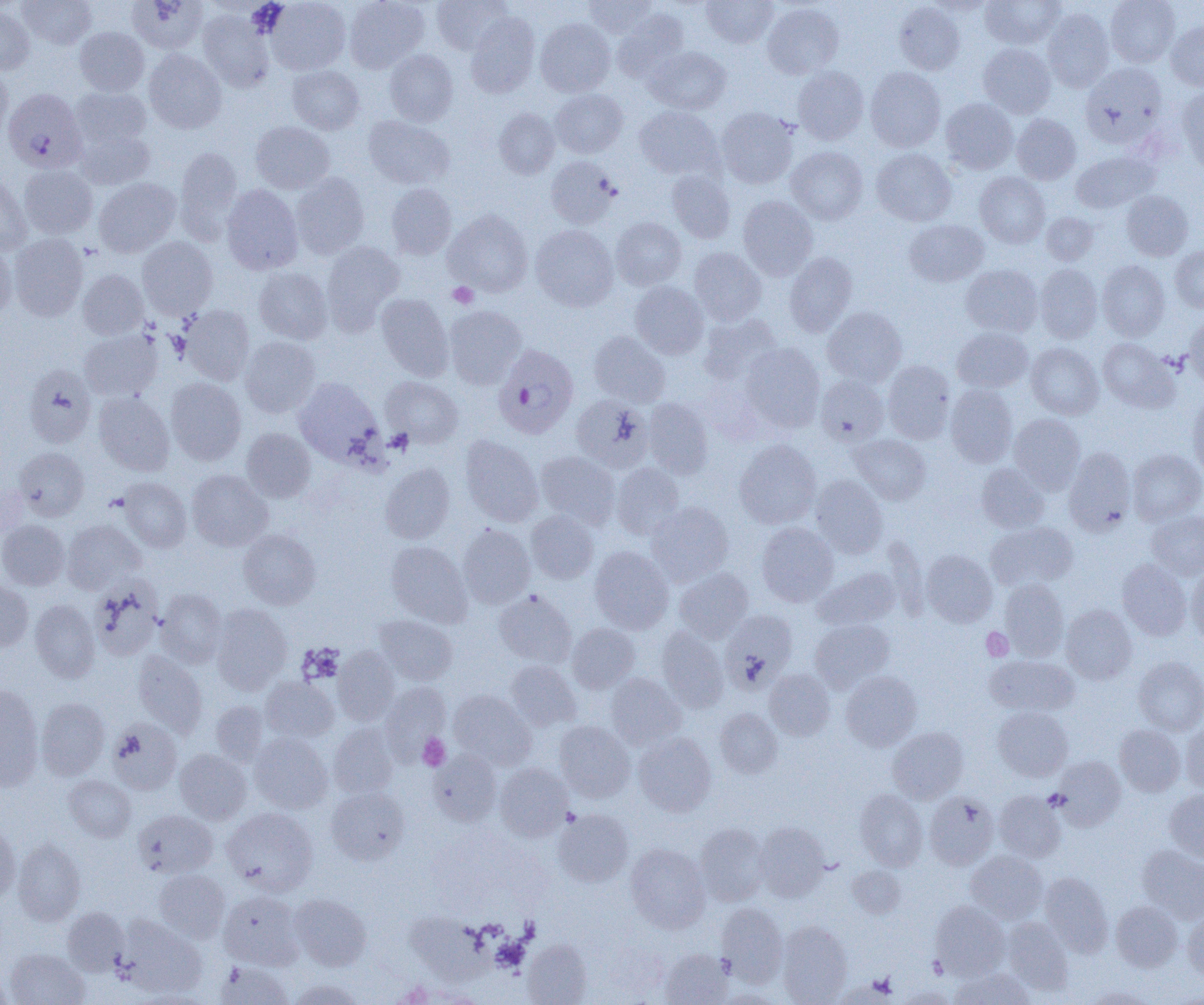
Summary:
  - Coordinate format: approximate bounding boxes as [x1, y1, x2, y2] in pixels
  - Platelet locations: [447, 282, 478, 309], [981, 627, 1013, 661], [417, 734, 450, 770], [1044, 789, 1068, 811], [859, 973, 899, 999]
  - Plasmodium falciparum-infected red blood cell locations: [3, 88, 87, 173], [493, 345, 579, 440]
  - Uninfected red blood cell locations: [17, 0, 96, 49], [127, 0, 208, 54], [265, 0, 350, 75], [345, 0, 429, 73], [432, 0, 511, 54], [582, 0, 659, 37], [700, 0, 778, 47], [927, 0, 994, 17], [980, 0, 1064, 49], [1105, 0, 1180, 67], [762, 2, 844, 79], [894, 2, 965, 74], [0, 5, 35, 74], [1042, 7, 1114, 92], [613, 8, 691, 83], [198, 10, 275, 92], [466, 13, 540, 97], [535, 18, 615, 96], [1166, 21, 1204, 91], [75, 27, 149, 95], [978, 43, 1056, 118], [646, 46, 731, 114], [144, 49, 226, 133], [385, 50, 458, 126], [1081, 63, 1167, 148], [0, 65, 13, 139], [287, 65, 364, 134], [792, 66, 869, 144], [865, 67, 946, 152], [70, 87, 152, 151], [550, 88, 627, 158], [1177, 88, 1204, 176], [941, 97, 1018, 174], [634, 106, 722, 179], [493, 107, 560, 179], [716, 107, 799, 188], [1012, 114, 1081, 184], [363, 116, 454, 189], [250, 121, 335, 194], [74, 127, 155, 189], [175, 146, 243, 238], [786, 146, 868, 224], [871, 148, 956, 226], [1071, 150, 1158, 213], [546, 156, 620, 228], [18, 164, 98, 239], [666, 170, 735, 243], [0, 172, 33, 255], [975, 172, 1050, 248], [291, 173, 369, 259], [94, 178, 181, 257], [386, 183, 457, 259], [221, 184, 303, 274], [1121, 190, 1193, 260], [738, 196, 818, 279], [443, 210, 533, 296], [1041, 212, 1099, 265], [610, 217, 686, 290], [904, 219, 988, 287], [530, 224, 618, 311], [9, 233, 88, 321], [137, 236, 218, 319], [0, 239, 17, 322], [321, 241, 405, 332], [1171, 246, 1204, 312], [689, 247, 766, 326], [784, 252, 857, 336], [1097, 260, 1170, 341], [961, 264, 1042, 336], [1035, 264, 1102, 343], [254, 267, 333, 344], [78, 270, 149, 340], [630, 281, 709, 358], [376, 293, 454, 381], [179, 305, 255, 385], [444, 305, 526, 389], [823, 307, 906, 387], [699, 313, 782, 385], [1184, 313, 1204, 388], [952, 327, 1033, 392], [79, 329, 162, 401], [589, 332, 670, 407], [240, 336, 320, 417], [1098, 338, 1177, 413], [741, 343, 825, 433], [1026, 343, 1103, 419], [882, 361, 954, 443], [23, 364, 97, 447], [815, 375, 888, 445], [381, 376, 464, 448], [294, 377, 382, 464], [166, 378, 246, 465], [945, 384, 1017, 467], [94, 391, 175, 475], [1187, 393, 1204, 480], [572, 395, 653, 472], [643, 398, 714, 478], [1009, 413, 1084, 494], [242, 428, 316, 502], [849, 434, 930, 505], [460, 435, 543, 526], [734, 439, 821, 529], [14, 447, 89, 520], [1064, 447, 1135, 535], [1128, 449, 1204, 525], [536, 451, 620, 528], [380, 463, 455, 543], [611, 463, 684, 539], [976, 463, 1050, 533], [186, 470, 273, 551], [810, 475, 888, 558], [119, 478, 192, 552], [646, 502, 733, 585], [526, 510, 599, 584], [1146, 510, 1204, 579], [61, 519, 146, 594], [0, 520, 69, 590], [986, 521, 1077, 591], [756, 522, 839, 607], [457, 524, 535, 608], [238, 529, 320, 609], [385, 541, 472, 627], [589, 546, 674, 634], [921, 549, 997, 627], [1117, 559, 1191, 640], [1186, 565, 1204, 646], [674, 567, 753, 641], [813, 567, 900, 631], [90, 575, 163, 660], [999, 579, 1069, 660], [0, 581, 33, 652], [155, 588, 227, 667], [493, 590, 577, 668], [30, 599, 99, 682], [211, 604, 292, 694], [1061, 605, 1137, 683], [720, 609, 797, 693], [374, 615, 457, 685], [810, 619, 894, 692], [567, 623, 640, 693], [656, 627, 729, 712], [333, 646, 400, 725], [132, 651, 208, 737], [985, 655, 1079, 717], [1133, 656, 1204, 735], [506, 661, 582, 730], [764, 669, 834, 740], [841, 671, 922, 751], [605, 673, 686, 749], [261, 676, 339, 742], [380, 682, 451, 759], [0, 685, 44, 790], [449, 690, 536, 770], [36, 698, 109, 779], [211, 701, 268, 766], [994, 706, 1072, 781], [715, 708, 782, 778], [107, 719, 182, 795], [1181, 719, 1204, 794], [554, 721, 634, 802], [328, 723, 398, 798], [1114, 724, 1185, 796], [888, 726, 969, 803], [250, 732, 332, 814], [634, 732, 716, 816], [175, 749, 251, 824], [429, 750, 502, 826], [1053, 755, 1126, 830], [495, 763, 572, 840], [63, 775, 136, 842], [326, 787, 409, 865], [855, 789, 928, 870], [1165, 789, 1204, 862], [924, 791, 998, 870], [994, 791, 1065, 862], [222, 808, 318, 895], [553, 809, 634, 887], [133, 810, 218, 878], [0, 818, 20, 902], [695, 823, 769, 906], [754, 823, 830, 902], [12, 838, 86, 925], [626, 844, 710, 933], [1138, 845, 1204, 924], [966, 850, 1049, 924], [847, 865, 906, 918], [154, 869, 230, 942], [1040, 872, 1112, 956], [218, 890, 304, 969], [290, 894, 371, 970], [931, 901, 1010, 979], [1111, 901, 1182, 971], [716, 903, 787, 985], [62, 907, 129, 974], [403, 910, 506, 988], [1183, 911, 1204, 981], [118, 915, 207, 997], [1001, 917, 1074, 995], [777, 921, 852, 1005], [523, 939, 591, 1005], [5, 948, 89, 1005], [660, 949, 733, 1004], [216, 961, 292, 1004], [950, 968, 1033, 1004], [0, 972, 12, 1004], [289, 978, 364, 1005], [897, 986, 959, 1004], [1083, 986, 1156, 1004], [717, 989, 788, 1005]
  - Slide-level diagnosis: Plasmodium falciparum
  - Preparation: thin blood smear
  - Magnification: 1000x
  - Image size: 1204×1005 pixels
  - Modality: optical microscopy
  - Field of view: single